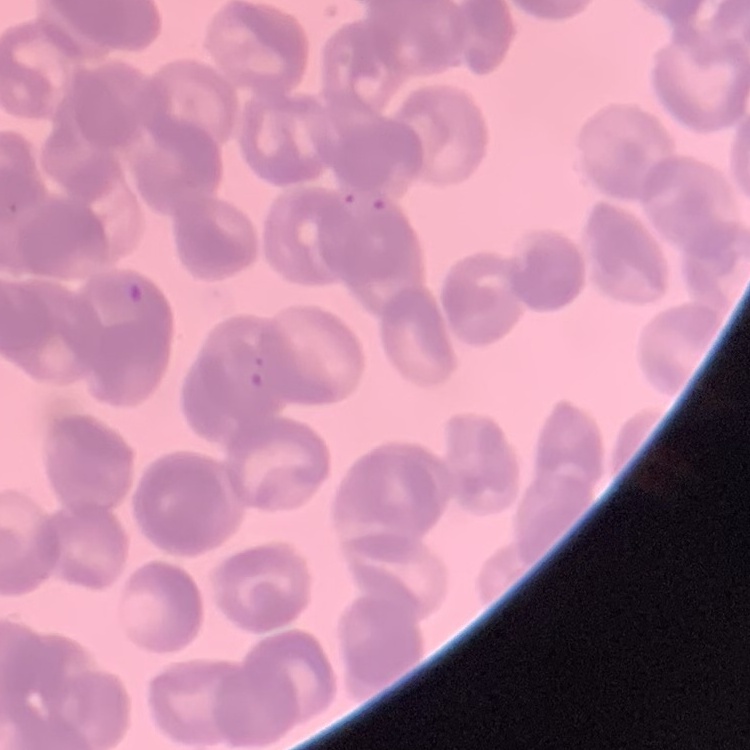 The red blood cells exhibit rouleaux formation. Field's or Giemsa stain. One tile cut from a larger photomicrograph. Thin blood film.